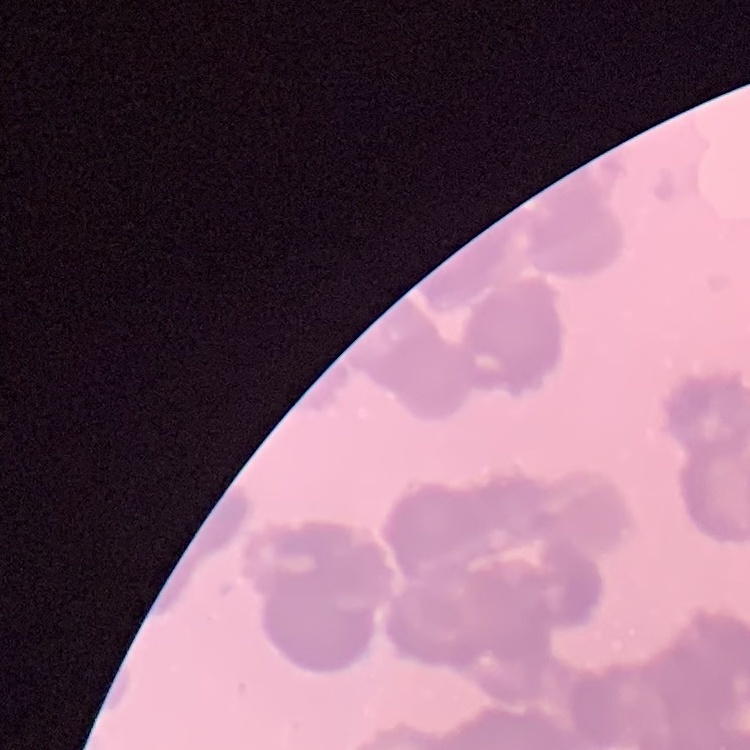

Summary:
  - Red blood cell morphology: rouleaux formation
  - Stain: Field's or Giemsa
  - Preparation: thin peripheral smear
  - Image type: one tile cut from a larger photomicrograph